Report the malaria status of this cell.
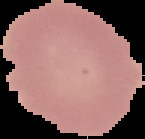

Uninfected.

image type = cell region segmented out of the field of view; surrounding area masked to black
preparation = thin blood film
image size = 145×139 pixels